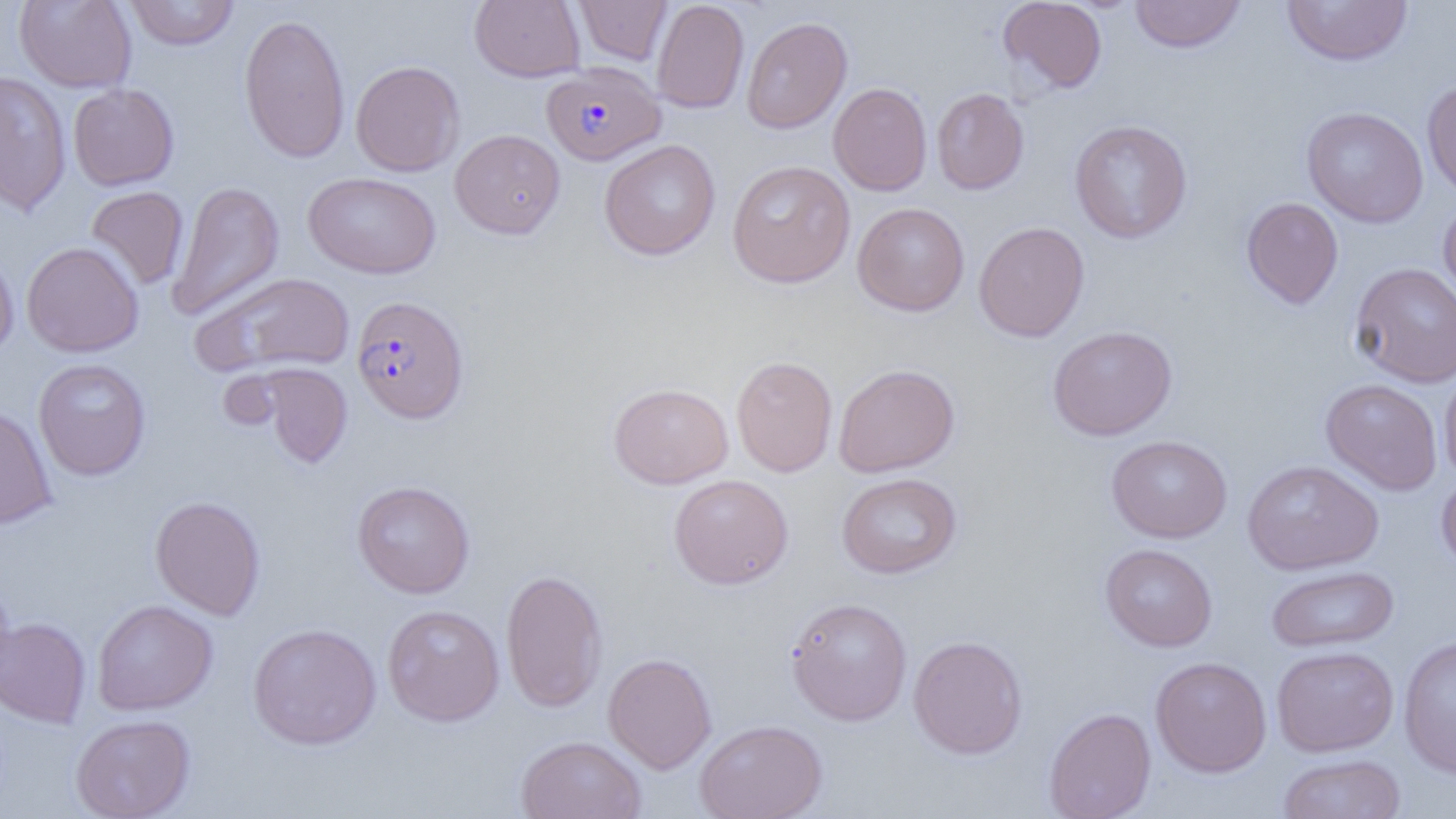
Summary:
  - Coordinate format: approximate bounding boxes as (x1,y1)-(x2,y2) corner pairs in pixels
  - Plasmodium falciparum-infected red blood cell locations: (542,62)-(665,166), (351,295)-(469,424)
  - Uninfected red blood cell locations: (14,0)-(137,92), (125,0)-(239,50), (469,0)-(585,82), (574,0)-(672,65), (651,0)-(749,114), (1129,0)-(1246,54), (1281,0)-(1413,67), (997,1)-(1108,94), (238,13)-(351,163), (741,16)-(852,134), (350,60)-(465,177), (0,71)-(72,217), (1422,80)-(1456,200), (828,82)-(932,196), (68,83)-(179,190), (931,88)-(1029,194), (1301,106)-(1429,228), (1069,119)-(1193,244), (449,129)-(565,239), (598,140)-(721,260), (727,160)-(855,288), (303,172)-(441,279), (168,180)-(285,321), (86,186)-(189,290), (1241,197)-(1344,310), (1438,198)-(1456,307), (852,202)-(969,316), (973,221)-(1090,342), (21,241)-(144,357), (0,245)-(19,360), (1349,261)-(1456,388), (192,271)-(355,376), (1047,325)-(1177,441), (731,355)-(838,477), (33,358)-(151,481), (255,363)-(353,469), (833,363)-(960,477), (1439,364)-(1456,484), (1320,378)-(1443,496), (608,382)-(733,489), (0,404)-(57,529), (1106,435)-(1232,543), (1243,459)-(1383,575), (1436,471)-(1456,576), (836,472)-(962,579), (668,474)-(794,590), (352,480)-(475,598), (150,495)-(265,620), (1100,543)-(1218,652), (1266,565)-(1399,654), (501,567)-(608,713), (785,596)-(913,726), (92,599)-(218,716), (382,604)-(505,726), (0,617)-(91,728), (248,622)-(382,750), (1398,634)-(1456,779), (908,635)-(1028,759), (1271,645)-(1399,757), (603,652)-(717,773), (1150,656)-(1272,778), (1043,707)-(1156,819), (70,714)-(196,819), (695,719)-(828,819), (514,735)-(647,818), (1277,753)-(1407,819)
  - Slide-level diagnosis: Plasmodium falciparum
  - Image size: 1456×819 pixels
  - Preparation: thin blood film
  - Magnification: 1000x
  - Field of view: one of a larger specimen
  - Modality: optical microscopy